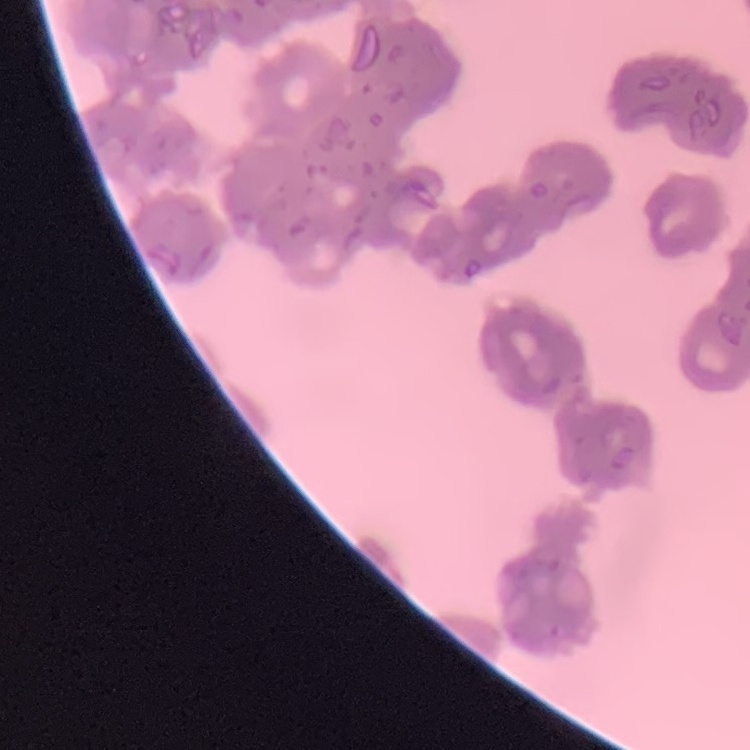

The erythrocytes exhibit rouleaux formation. One tile cut from a larger photomicrograph. Field's or Giemsa stain. Thin peripheral smear.